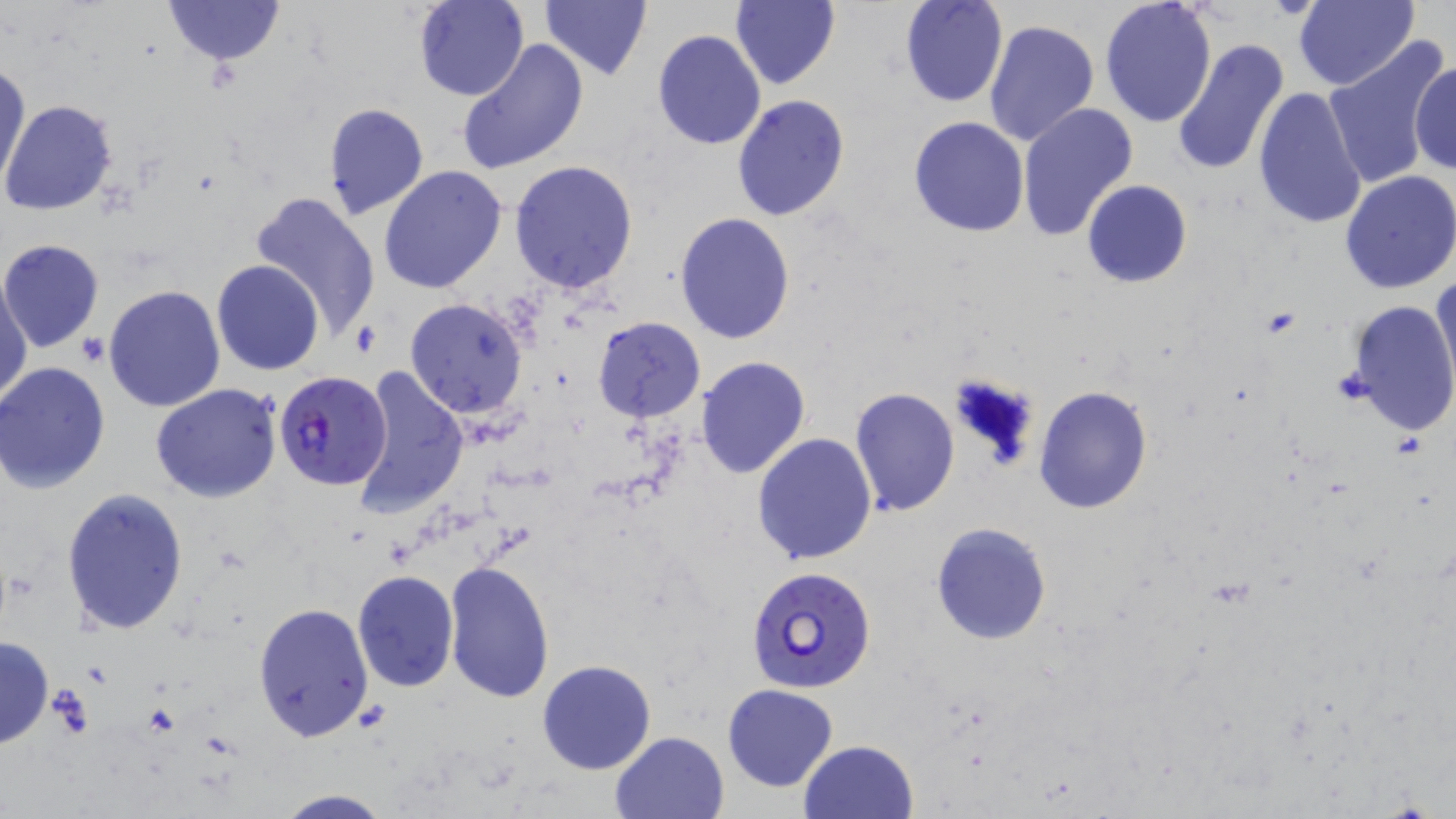

Approximate bounding boxes as (x1,y1)-(x2,y2) corner pairs in pixels. Uninfected red blood cell locations: (161,0)-(286,65), (412,0)-(528,101), (729,0)-(840,89), (900,0)-(1008,107), (1099,0)-(1217,125), (1294,0)-(1420,92), (539,1)-(653,79), (984,18)-(1098,147), (651,29)-(766,150), (1324,37)-(1455,189), (1171,38)-(1291,176), (456,39)-(588,177), (1412,57)-(1454,179), (1,62)-(29,190), (1251,87)-(1368,230), (732,94)-(850,222), (2,101)-(117,216), (322,103)-(430,221), (1017,103)-(1138,241), (907,116)-(1030,238), (508,160)-(639,295), (378,166)-(508,295), (1340,170)-(1456,294), (1081,179)-(1193,288), (249,191)-(382,339), (674,213)-(795,343), (0,240)-(105,353), (212,259)-(323,375), (1431,271)-(1455,390), (1,279)-(32,407), (103,284)-(227,413), (404,298)-(530,420), (1345,300)-(1456,436), (593,318)-(705,421), (694,356)-(810,479), (0,363)-(111,493), (352,367)-(468,519), (150,383)-(282,503), (1032,385)-(1152,514), (849,388)-(960,516), (752,432)-(878,566), (60,489)-(189,636), (930,523)-(1052,645), (444,561)-(554,704), (352,571)-(459,692), (253,602)-(374,743), (0,634)-(52,750), (537,660)-(657,774), (722,684)-(838,791), (608,731)-(730,819), (798,740)-(919,819), (269,789)-(395,819). Plasmodium falciparum-infected red blood cell locations: (276,371)-(393,490), (746,565)-(878,694). Platelet locations: (79,334)-(112,367). Slide-level diagnosis: Plasmodium falciparum. Captured at 1000x magnification. Optical microscopy. Single field of view. Thin blood film. May-Grünwald-Giemsa stain. Image is 1456×819 pixels.